Describe the morphology of the erythrocytes.
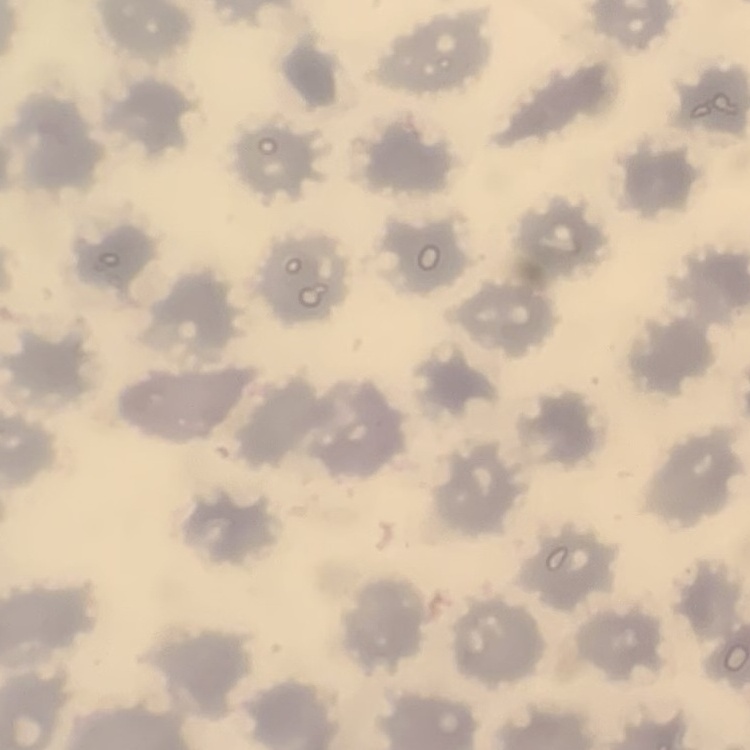

They show no rouleaux formation.

{
  "stain": "Field's or Giemsa",
  "preparation": "thin blood smear",
  "image_type": "square crop of a larger photomicrograph"
}